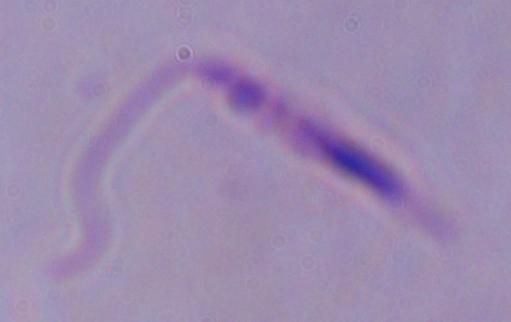

Captured at 1000x magnification. A Leishmania parasite is shown. Photomicrograph.